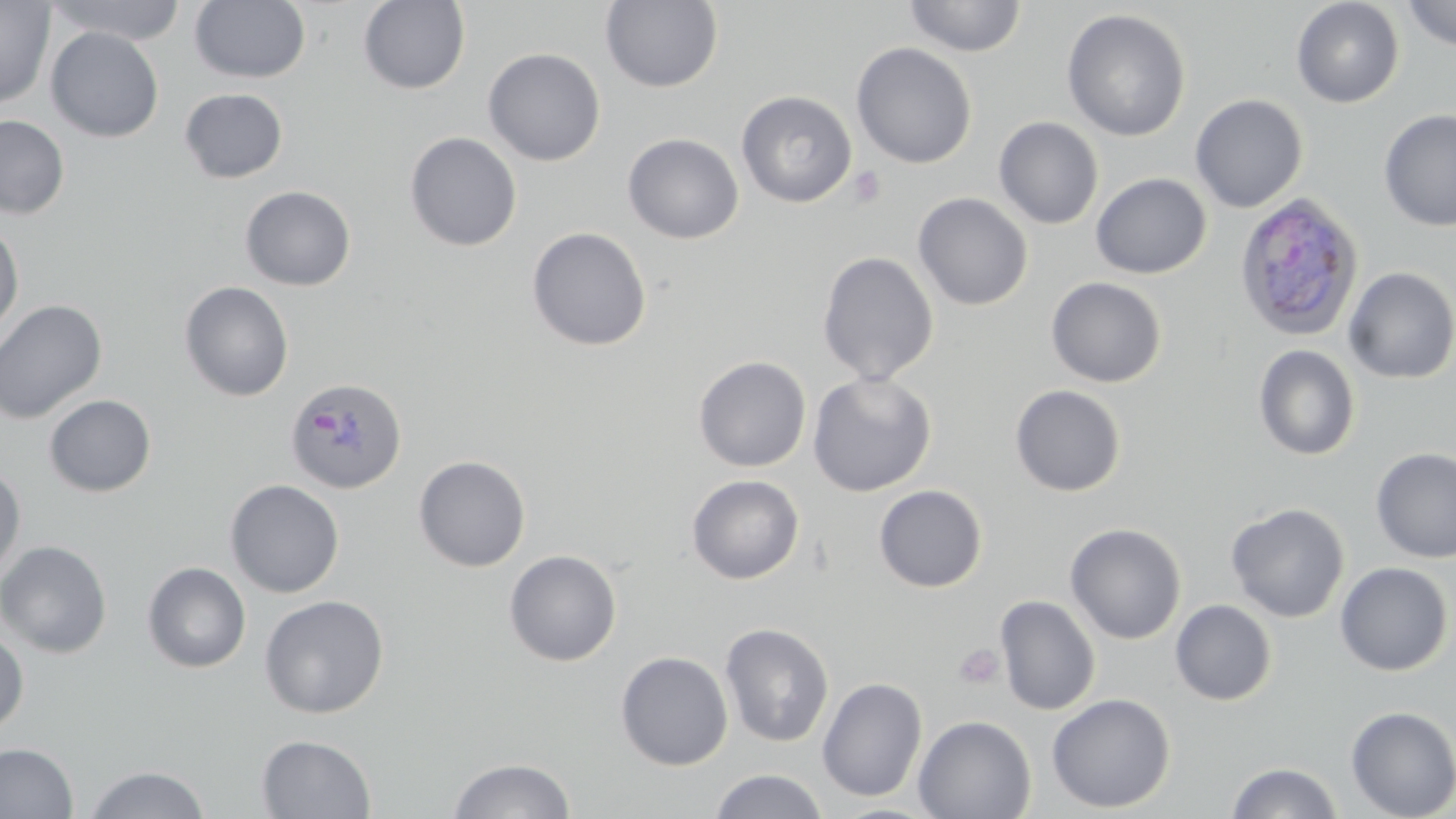
Plasmodium ovale-infected red blood cell locations = approximate bounding boxes as (x1,y1)-(x2,y2) corner pairs in pixels: (1234,192)-(1368,341), (285,377)-(408,495)
slide-level diagnosis = Plasmodium ovale
platelet locations = approximate bounding boxes as (x1,y1)-(x2,y2) corner pairs in pixels: (846,167)-(885,208), (954,643)-(1004,690)
field of view = one of a larger specimen
image size = 1456×819 pixels
preparation = thin blood smear
uninfected red blood cell locations = approximate bounding boxes as (x1,y1)-(x2,y2) corner pairs in pixels: (45,0)-(189,45), (190,0)-(311,84), (903,0)-(1028,57), (1291,0)-(1404,108), (0,1)-(55,107), (358,1)-(471,94), (600,1)-(724,92), (1400,1)-(1456,51), (1062,8)-(1191,142), (46,26)-(164,142), (851,41)-(978,169), (482,47)-(605,166), (179,88)-(288,183), (736,90)-(857,207), (1190,94)-(1308,213), (1378,108)-(1455,231), (0,114)-(70,219), (993,117)-(1104,230), (404,132)-(522,251), (622,132)-(744,244), (1090,173)-(1211,279), (239,185)-(356,291), (913,192)-(1033,311), (0,222)-(24,337), (526,226)-(652,351), (817,251)-(939,385), (1343,266)-(1456,384), (1046,276)-(1167,388), (178,281)-(294,401), (0,299)-(107,424), (1253,344)-(1361,461), (693,355)-(811,472), (807,371)-(937,496), (1010,385)-(1127,497), (43,394)-(157,497), (1370,447)-(1456,563), (413,455)-(531,572), (0,463)-(26,581), (686,474)-(804,584), (224,479)-(345,598), (873,484)-(988,593), (1226,502)-(1350,623), (1065,523)-(1186,644), (0,540)-(112,658), (503,549)-(622,666), (142,561)-(251,673), (1334,562)-(1453,675), (995,594)-(1101,716), (259,595)-(390,719), (1170,599)-(1277,706), (719,622)-(834,748), (0,627)-(29,735), (615,650)-(734,771), (817,677)-(928,801), (1046,693)-(1176,813), (1345,706)-(1456,819), (913,714)-(1037,819), (256,734)-(376,818), (0,742)-(79,819), (448,757)-(576,818), (1226,761)-(1343,819), (84,764)-(210,818), (709,769)-(829,819)
stain = May-Grünwald-Giemsa
modality = optical microscopy
magnification = 1000x